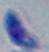

Summary:
  - Identification: Toxoplasma gondii
  - Modality: micrograph
  - Magnification: 1000x